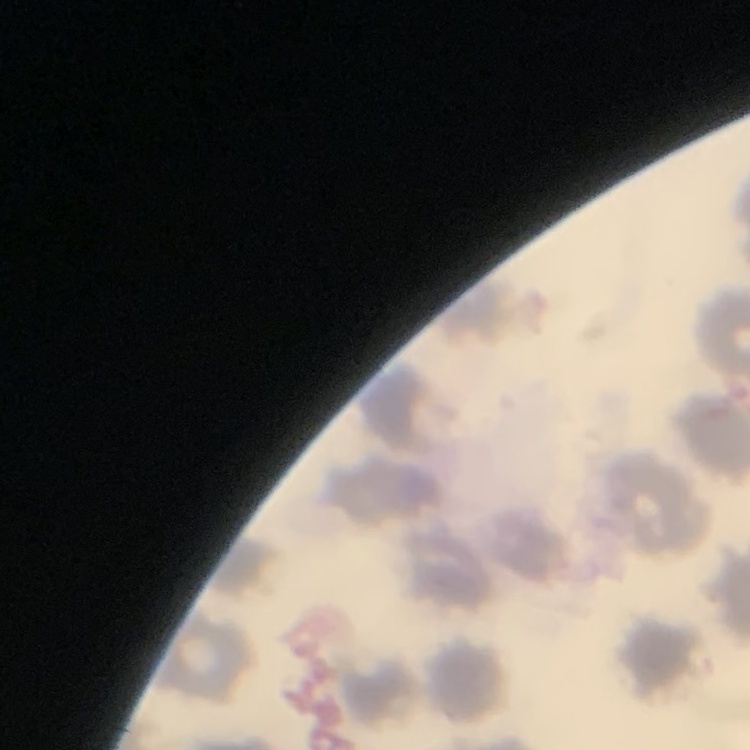
The erythrocytes exhibit no rouleaux formation. Square crop of a larger photomicrograph. Stained with either Field's or Giemsa. Thin blood smear.